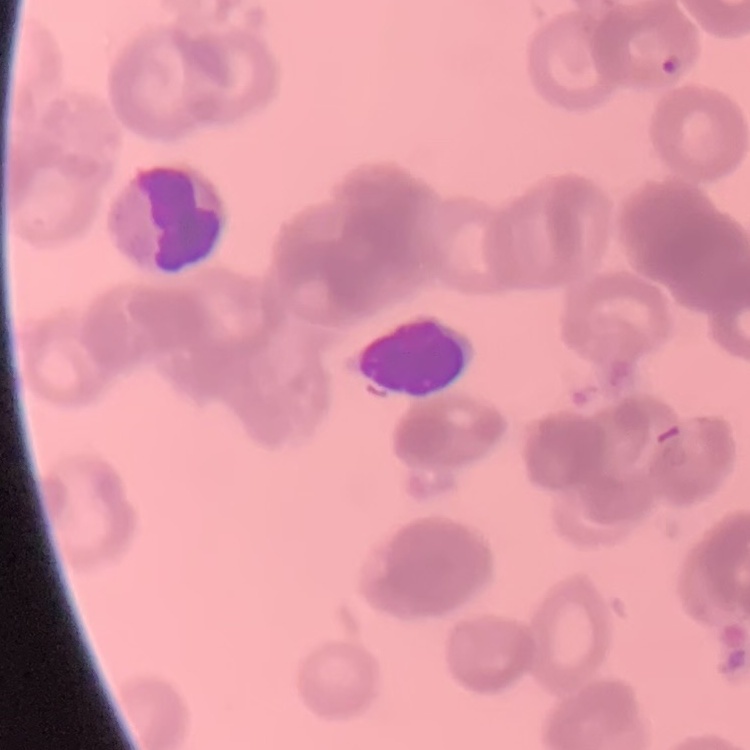
red blood cell morphology = rouleaux formation
stain = Field's or Giemsa
image type = one tile cut from a larger photomicrograph
preparation = thin blood smear